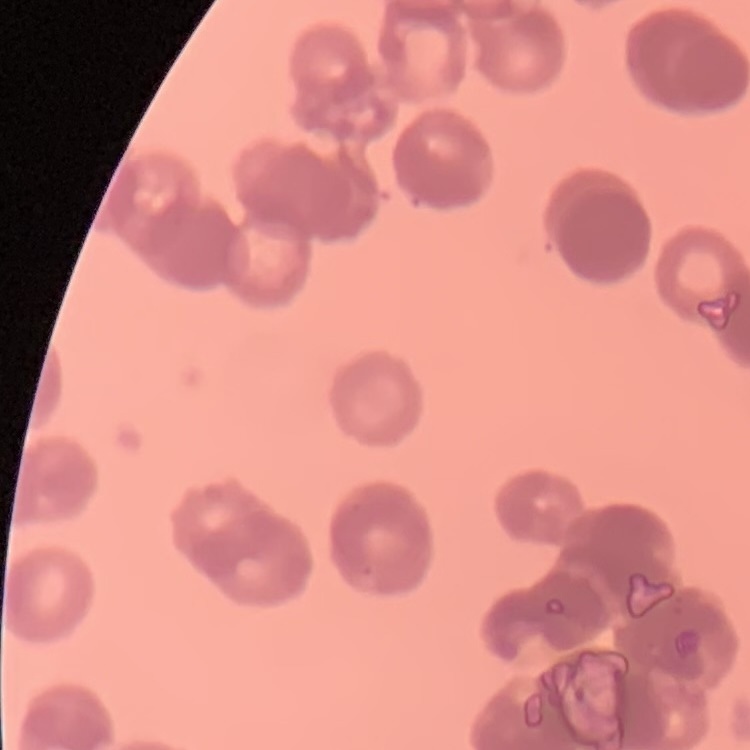

erythrocyte morphology = rouleaux formation
image type = one tile cut from a larger photomicrograph
stain = Field's or Giemsa
preparation = thin peripheral smear